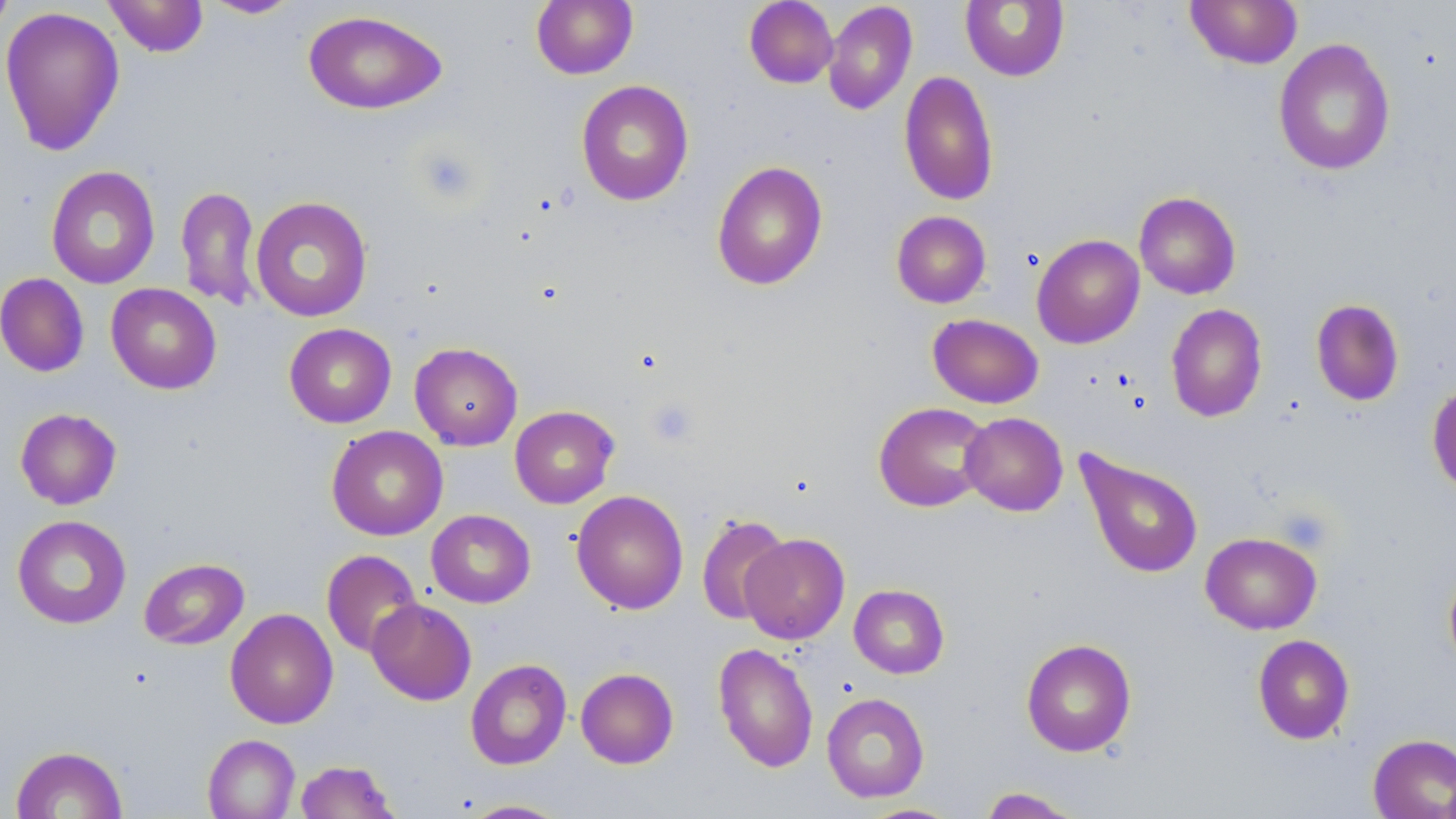
Approximate bounding boxes as (x1,y1)-(x2,y2) corner pairs in pixels. Uninfected red blood cell locations: (0,0)-(15,37), (103,0)-(209,58), (201,0)-(303,19), (531,0)-(638,79), (744,0)-(838,89), (1185,0)-(1303,69), (822,1)-(917,115), (960,1)-(1070,81), (0,6)-(125,157), (302,9)-(447,115), (1273,38)-(1395,175), (898,70)-(999,206), (576,80)-(694,206), (711,160)-(828,291), (45,165)-(160,289), (175,186)-(261,310), (1134,191)-(1241,299), (250,196)-(373,323), (891,211)-(991,308), (1032,234)-(1145,349), (0,273)-(90,377), (105,283)-(222,395), (1310,298)-(1405,406), (1166,303)-(1268,423), (928,314)-(1044,409), (284,323)-(396,428), (409,342)-(522,450), (1427,381)-(1456,496), (873,402)-(992,512), (509,405)-(619,508), (14,408)-(122,509), (960,412)-(1068,516), (326,425)-(448,541), (1075,448)-(1204,579), (571,490)-(688,614), (426,509)-(535,608), (696,513)-(792,626), (12,514)-(131,629), (1200,531)-(1322,634), (740,533)-(850,644), (321,549)-(422,657), (139,558)-(249,650), (1443,562)-(1456,674), (849,584)-(949,679), (366,598)-(477,705), (225,608)-(338,729), (1252,634)-(1355,744), (1021,638)-(1137,757), (714,642)-(819,773), (465,658)-(572,770), (575,667)-(679,769), (822,692)-(929,803), (1367,733)-(1456,818), (203,734)-(300,819), (11,745)-(127,819), (294,760)-(400,819), (977,787)-(1086,818), (460,799)-(571,818), (858,803)-(963,818). Platelet locations: (415,146)-(481,206), (646,397)-(700,448). Slide-level diagnosis: negative for blood parasites. May-Grünwald-Giemsa stain. Light microscopy. Thin blood film. Image is 1456×819 pixels. One field of a larger specimen. 1000x magnification.